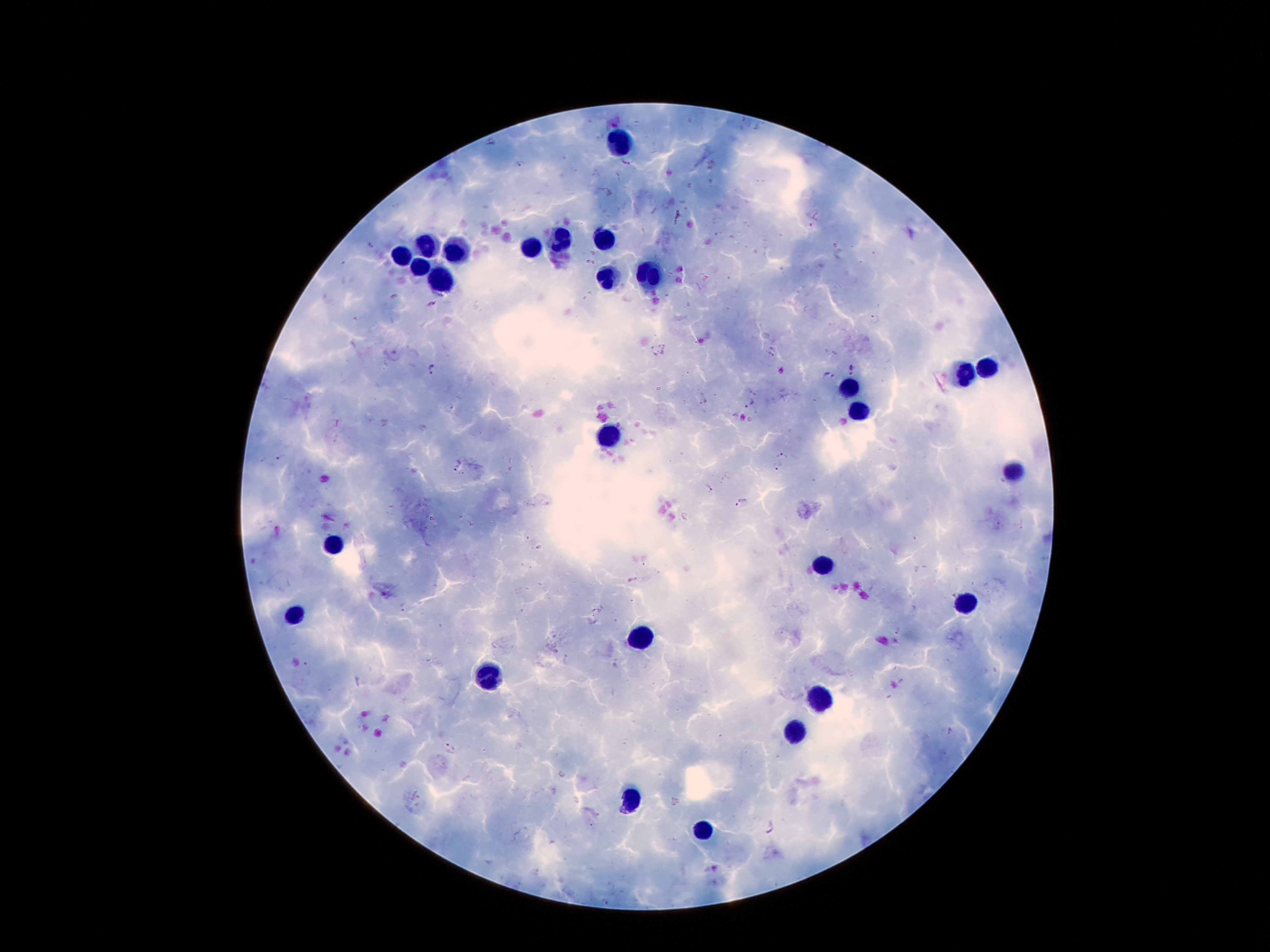

Approximate centers as {x, y} in pixels.
Summary:
  - Malaria parasite locations: {491, 141}, {520, 164}, {626, 164}, {370, 244}, {875, 319}, {664, 349}, {650, 352}, {769, 356}, {432, 368}, {851, 368}, {829, 376}, {750, 404}, {450, 408}, {782, 453}, {280, 458}, {777, 465}, {456, 469}, {710, 488}, {741, 503}, {402, 608}, {451, 749}, {769, 827}
  - Leukocyte locations: {617, 143}, {560, 239}, {601, 239}, {530, 247}, {426, 248}, {456, 250}, {404, 254}, {421, 268}, {648, 273}, {446, 279}, {606, 280}, {985, 370}, {962, 375}, {850, 391}, {857, 411}, {606, 436}, {1012, 470}, {333, 545}, {823, 561}, {966, 602}, {292, 613}, {640, 638}, {487, 675}, {825, 695}, {794, 729}, {633, 800}, {703, 831}
  - Stain: Giemsa
  - Preparation: thick peripheral-blood smear
  - Image size: 1270×952 pixels
  - Magnification: 100x
  - Patient malaria status: infected with Plasmodium falciparum
  - Capture: smartphone camera through the microscope eyepiece
  - Field of view: one from this slide